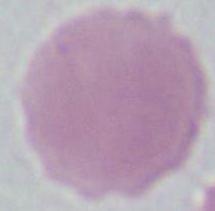
Summary:
  - Magnification: 1000x
  - Modality: photomicrograph
  - Identification: red blood cell